Identify the blood parasite species.
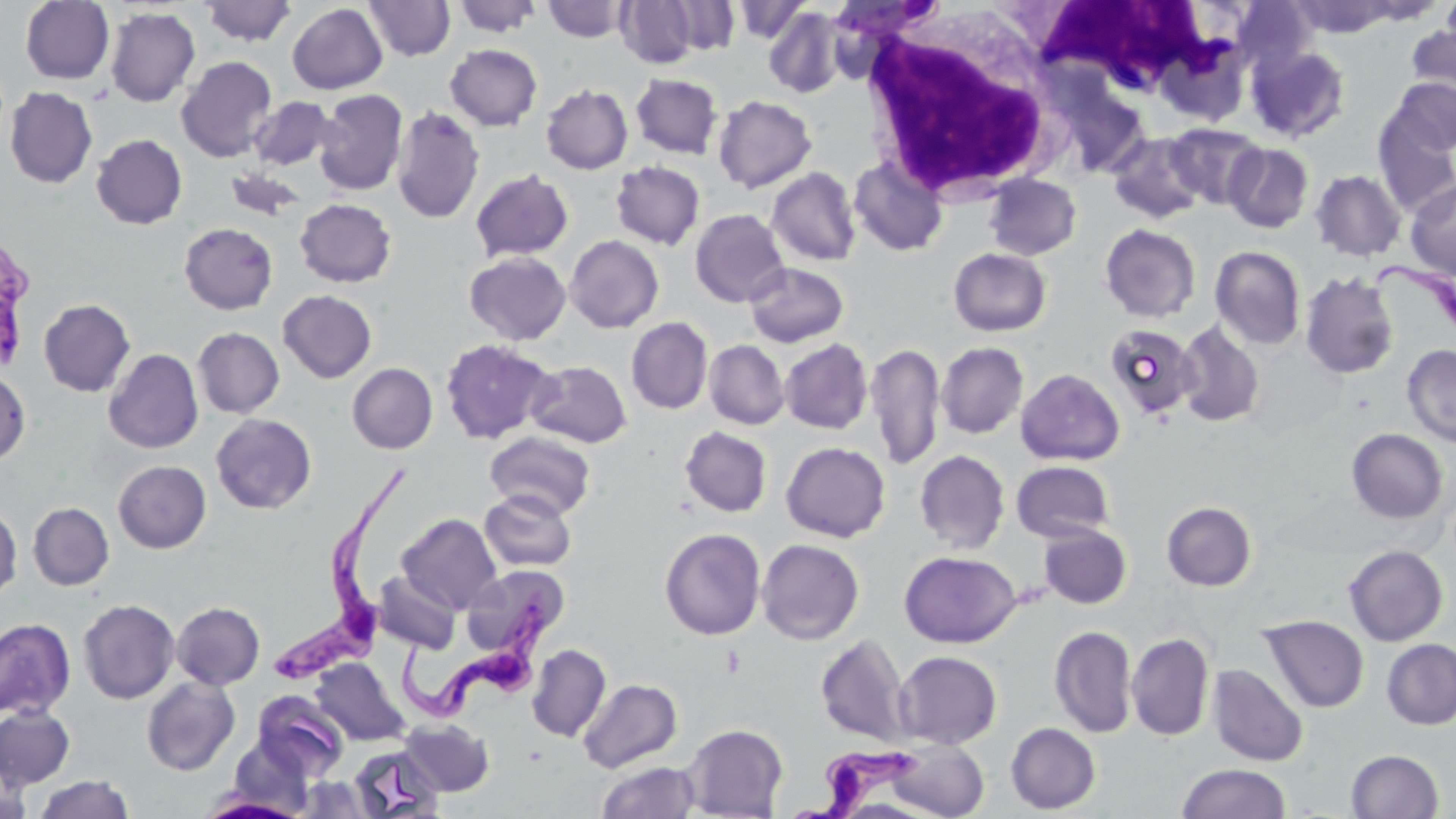
Trypanosoma brucei.

{
  "field_of_view": "one of a larger specimen",
  "stain": "May-Grünwald-Giemsa",
  "uninfected_red_blood_cell_locations": "approximate bounding boxes as named x1/y1/x2/y2 corners in pixels: (x1=20, y1=0, x2=114, y2=84), (x1=363, y1=0, x2=456, y2=60), (x1=452, y1=0, x2=543, y2=37), (x1=616, y1=0, x2=699, y2=68), (x1=666, y1=0, x2=740, y2=55), (x1=828, y1=0, x2=940, y2=44), (x1=1440, y1=0, x2=1456, y2=57), (x1=200, y1=1, x2=297, y2=46), (x1=542, y1=1, x2=631, y2=42), (x1=733, y1=1, x2=810, y2=44), (x1=1233, y1=1, x2=1316, y2=74), (x1=287, y1=3, x2=387, y2=94), (x1=105, y1=7, x2=200, y2=107), (x1=763, y1=7, x2=845, y2=98), (x1=1405, y1=22, x2=1456, y2=110), (x1=445, y1=44, x2=542, y2=131), (x1=1246, y1=44, x2=1352, y2=143), (x1=176, y1=56, x2=277, y2=162), (x1=630, y1=73, x2=722, y2=159), (x1=1388, y1=78, x2=1455, y2=157), (x1=541, y1=84, x2=633, y2=174), (x1=4, y1=87, x2=98, y2=188), (x1=314, y1=89, x2=408, y2=196), (x1=713, y1=95, x2=817, y2=193), (x1=249, y1=97, x2=336, y2=170), (x1=391, y1=106, x2=485, y2=224), (x1=1372, y1=108, x2=1456, y2=217), (x1=1165, y1=123, x2=1266, y2=210), (x1=1107, y1=131, x2=1208, y2=224), (x1=91, y1=134, x2=187, y2=229), (x1=1223, y1=142, x2=1314, y2=233), (x1=849, y1=156, x2=948, y2=257), (x1=610, y1=161, x2=705, y2=249), (x1=226, y1=167, x2=307, y2=223), (x1=767, y1=167, x2=861, y2=266), (x1=470, y1=168, x2=573, y2=262), (x1=1310, y1=169, x2=1406, y2=261), (x1=984, y1=174, x2=1081, y2=260), (x1=1405, y1=180, x2=1456, y2=279), (x1=295, y1=198, x2=396, y2=287), (x1=690, y1=208, x2=789, y2=307), (x1=179, y1=222, x2=278, y2=314), (x1=1100, y1=223, x2=1201, y2=323), (x1=565, y1=235, x2=664, y2=333), (x1=1210, y1=246, x2=1306, y2=349), (x1=948, y1=247, x2=1051, y2=336), (x1=464, y1=252, x2=571, y2=345), (x1=744, y1=262, x2=848, y2=347), (x1=1300, y1=271, x2=1400, y2=379), (x1=278, y1=290, x2=377, y2=383), (x1=38, y1=298, x2=135, y2=397), (x1=626, y1=317, x2=713, y2=414), (x1=1175, y1=321, x2=1264, y2=428), (x1=1105, y1=322, x2=1199, y2=421), (x1=192, y1=327, x2=284, y2=418), (x1=440, y1=339, x2=557, y2=444), (x1=780, y1=339, x2=873, y2=434), (x1=704, y1=340, x2=789, y2=429), (x1=936, y1=341, x2=1029, y2=439), (x1=866, y1=342, x2=945, y2=469), (x1=1402, y1=344, x2=1456, y2=447), (x1=103, y1=348, x2=203, y2=453), (x1=527, y1=359, x2=632, y2=447), (x1=347, y1=363, x2=438, y2=454), (x1=1016, y1=369, x2=1125, y2=466), (x1=0, y1=370, x2=30, y2=465), (x1=211, y1=413, x2=317, y2=514), (x1=680, y1=426, x2=772, y2=517), (x1=1346, y1=428, x2=1448, y2=524), (x1=485, y1=431, x2=596, y2=519), (x1=781, y1=442, x2=890, y2=542), (x1=914, y1=450, x2=1010, y2=554), (x1=113, y1=460, x2=211, y2=553), (x1=1011, y1=461, x2=1115, y2=543), (x1=479, y1=490, x2=577, y2=572), (x1=1161, y1=501, x2=1257, y2=591), (x1=28, y1=502, x2=114, y2=590), (x1=0, y1=504, x2=22, y2=602), (x1=396, y1=513, x2=502, y2=614), (x1=1038, y1=524, x2=1132, y2=609), (x1=660, y1=527, x2=766, y2=640), (x1=756, y1=538, x2=864, y2=645), (x1=1343, y1=545, x2=1448, y2=646), (x1=899, y1=550, x2=1021, y2=648), (x1=460, y1=564, x2=568, y2=658), (x1=373, y1=571, x2=461, y2=654), (x1=78, y1=599, x2=179, y2=704), (x1=172, y1=602, x2=265, y2=690), (x1=1259, y1=615, x2=1369, y2=713), (x1=0, y1=618, x2=76, y2=720), (x1=1049, y1=626, x2=1137, y2=737), (x1=1126, y1=632, x2=1214, y2=741), (x1=816, y1=634, x2=912, y2=746), (x1=1382, y1=638, x2=1456, y2=730), (x1=527, y1=644, x2=611, y2=742), (x1=895, y1=650, x2=1002, y2=749), (x1=311, y1=657, x2=410, y2=746), (x1=1208, y1=664, x2=1308, y2=767), (x1=142, y1=676, x2=240, y2=776), (x1=578, y1=678, x2=682, y2=773), (x1=252, y1=690, x2=349, y2=780), (x1=0, y1=705, x2=74, y2=788), (x1=399, y1=719, x2=495, y2=796), (x1=682, y1=723, x2=788, y2=818), (x1=1006, y1=723, x2=1100, y2=814), (x1=223, y1=738, x2=313, y2=816), (x1=887, y1=739, x2=989, y2=818), (x1=348, y1=745, x2=446, y2=818), (x1=1346, y1=749, x2=1444, y2=818), (x1=1, y1=759, x2=32, y2=819), (x1=596, y1=761, x2=702, y2=818), (x1=1176, y1=762, x2=1291, y2=819), (x1=34, y1=774, x2=134, y2=819), (x1=296, y1=776, x2=374, y2=818), (x1=197, y1=795, x2=308, y2=819)",
  "magnification": "1000x",
  "modality": "optical microscopy",
  "image_size": "1456×819 pixels",
  "trypanosoma_brucei_locations": "approximate bounding boxes as named x1/y1/x2/y2 corners in pixels: (x1=0, y1=228, x2=37, y2=376), (x1=1369, y1=259, x2=1456, y2=337), (x1=267, y1=463, x2=408, y2=686), (x1=398, y1=586, x2=555, y2=727), (x1=791, y1=745, x2=920, y2=819)",
  "white_blood_cell_locations": "approximate bounding boxes as named x1/y1/x2/y2 corners in pixels: (x1=1035, y1=0, x2=1233, y2=96), (x1=859, y1=12, x2=1058, y2=202)",
  "preparation": "thin blood smear"
}